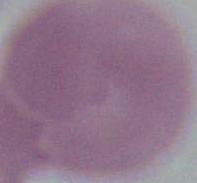
Summary:
  - Magnification: 1000x
  - Modality: micrograph
  - Identification: red blood cell